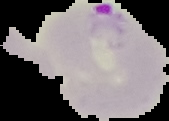
Image is 169×121 pixels. Segmented cell region on a black background. Result: Plasmodium parasites detected. From a thin blood smear.